Classify this cell by malaria status.
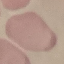
It is uninfected.

capture: smartphone through the microscope eyepiece
image_type: cell patch, automatically extracted from a larger field of view and resized to 64 × 64 pixels
preparation: thin blood film
stain: Giemsa